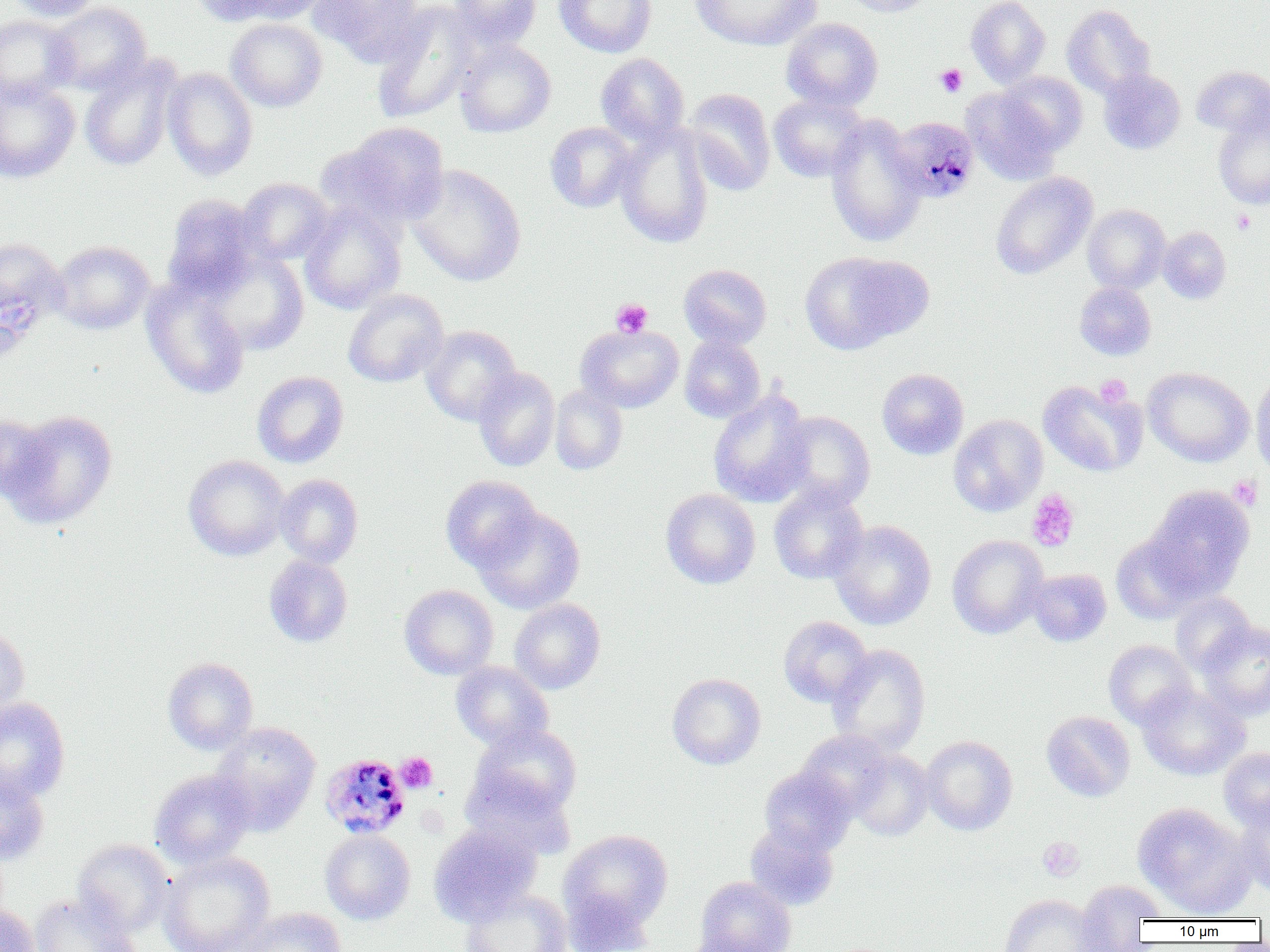
Summary:
  - Coordinate format: approximate bounding boxes as (x1, y1, x2, y2) in pixels
  - Platelet locations: (935, 64, 967, 97), (1231, 209, 1256, 235), (611, 298, 653, 337), (1095, 374, 1132, 408), (1229, 475, 1263, 511), (1026, 489, 1080, 551), (397, 752, 438, 793), (1037, 836, 1084, 882)
  - Plasmodium malariae-infected red blood cell locations: (891, 118, 982, 202), (320, 753, 410, 839)
  - Uninfected red blood cell locations: (5, 0, 104, 21), (192, 0, 288, 26), (232, 0, 330, 24), (309, 0, 425, 66), (449, 0, 541, 49), (553, 0, 657, 58), (691, 0, 820, 50), (838, 0, 934, 17), (965, 0, 1050, 88), (46, 2, 152, 95), (372, 3, 478, 123), (1062, 5, 1155, 97), (0, 15, 78, 103), (781, 18, 883, 112), (226, 19, 326, 112), (455, 39, 556, 137), (595, 53, 689, 146), (79, 59, 179, 172), (1192, 65, 1270, 138), (162, 68, 258, 180), (1098, 70, 1185, 154), (999, 72, 1088, 154), (0, 79, 81, 183), (963, 88, 1060, 184), (684, 89, 776, 195), (769, 93, 869, 182), (825, 115, 926, 248), (1213, 117, 1270, 209), (545, 121, 637, 212), (333, 122, 449, 228), (614, 124, 715, 249), (406, 164, 527, 286), (990, 172, 1097, 279), (236, 177, 335, 265), (161, 194, 264, 299), (299, 201, 406, 315), (1083, 204, 1171, 293), (1158, 226, 1231, 304), (0, 236, 68, 345), (51, 240, 155, 334), (206, 252, 308, 356), (799, 252, 916, 354), (678, 264, 772, 349), (142, 281, 249, 399), (1075, 282, 1156, 360), (343, 289, 448, 387), (421, 325, 521, 425), (576, 325, 684, 412), (680, 335, 765, 423), (1143, 367, 1254, 467), (473, 368, 560, 472), (876, 368, 969, 459), (1251, 370, 1270, 479), (252, 371, 349, 468), (1038, 380, 1147, 477), (550, 384, 628, 475), (708, 389, 814, 508), (2, 410, 118, 529), (774, 411, 875, 510), (0, 413, 53, 502), (949, 415, 1047, 516), (184, 455, 289, 561), (274, 474, 363, 568), (440, 475, 542, 573), (769, 484, 868, 584), (1145, 485, 1255, 598), (661, 488, 760, 589), (474, 506, 585, 614), (829, 520, 936, 630), (1111, 532, 1203, 624), (947, 535, 1048, 638), (264, 555, 353, 647), (1027, 568, 1111, 646), (399, 584, 498, 680), (1170, 592, 1255, 675), (509, 598, 605, 694), (778, 616, 873, 707), (1196, 621, 1270, 721), (0, 622, 30, 716), (1103, 640, 1197, 728), (827, 644, 931, 757), (162, 657, 258, 754), (450, 661, 553, 751), (667, 673, 766, 769), (1136, 683, 1250, 781), (0, 697, 70, 803), (1041, 711, 1136, 801), (211, 722, 322, 832), (470, 724, 582, 816), (796, 729, 894, 817), (921, 736, 1018, 835), (1219, 747, 1270, 830), (846, 749, 935, 842), (759, 765, 856, 856), (0, 769, 50, 866), (149, 769, 255, 869), (460, 769, 577, 860), (1132, 802, 1255, 916), (1235, 803, 1270, 896), (429, 822, 542, 925), (745, 823, 838, 911), (320, 829, 415, 925), (559, 829, 673, 933), (72, 838, 174, 937), (157, 851, 275, 952), (695, 876, 796, 952), (1074, 878, 1165, 945), (460, 890, 571, 952), (562, 891, 656, 952), (30, 893, 139, 952), (999, 894, 1102, 952), (0, 903, 40, 952), (239, 906, 346, 952), (682, 933, 775, 952)
  - Slide-level diagnosis: Plasmodium malariae
  - Preparation: thin blood smear
  - Magnification: 1000x
  - Field of view: single
  - Image size: 1270×952 pixels
  - Modality: light microscopy